Name the parasite shown.
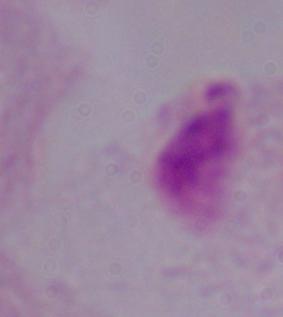

This is a trichomonad.

modality = micrograph
magnification = 1000x